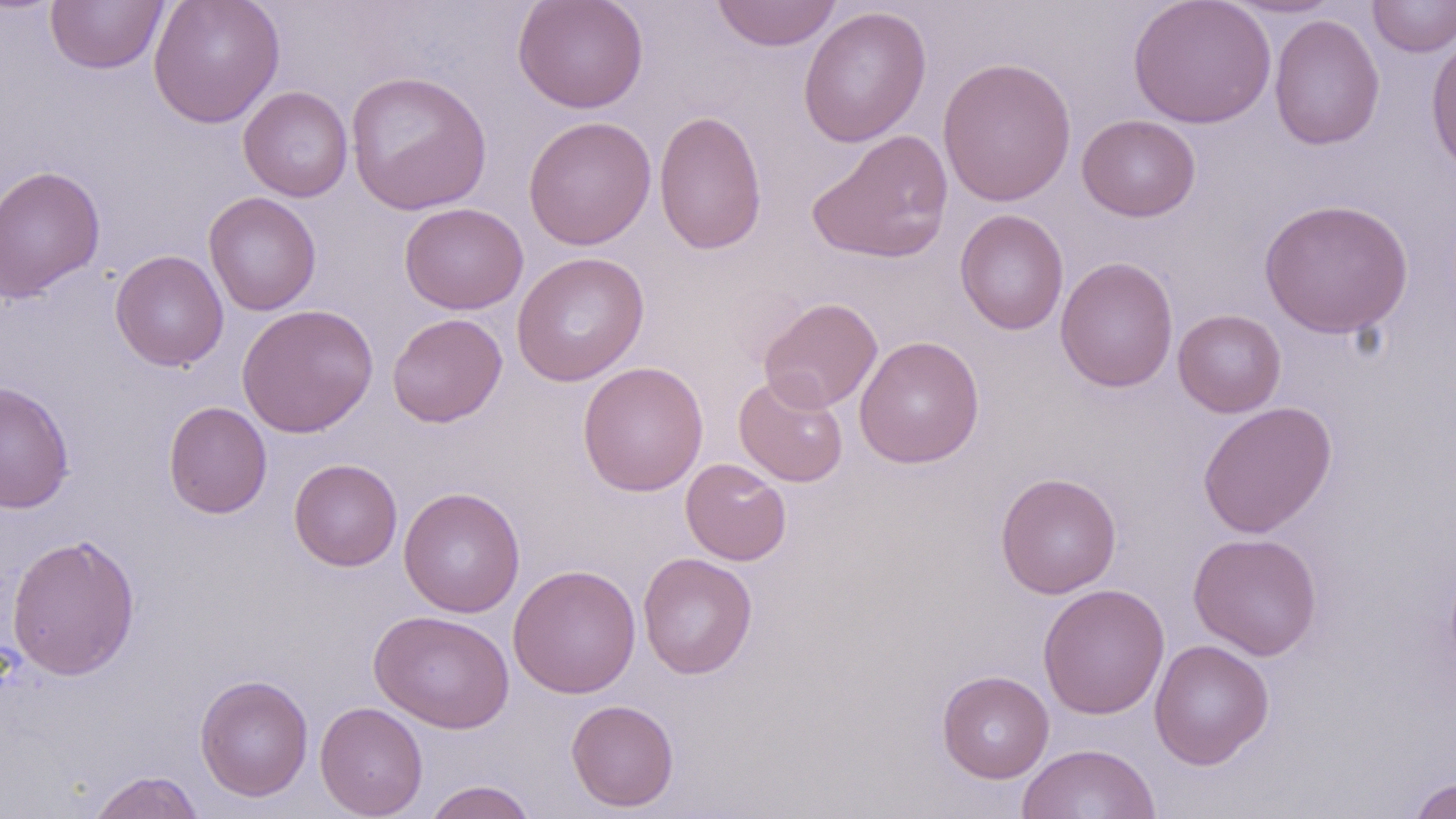 Approximate bounding boxes as [x1, y1, x2, y2] in pixels. Uninfected red blood cell locations: [148, 0, 285, 127], [513, 0, 649, 114], [710, 0, 843, 51], [1128, 0, 1276, 128], [1223, 0, 1343, 19], [1367, 0, 1456, 57], [46, 1, 168, 74], [797, 6, 932, 147], [1269, 14, 1385, 150], [1425, 34, 1456, 179], [937, 56, 1076, 207], [345, 70, 492, 215], [238, 85, 353, 202], [653, 109, 768, 256], [1077, 114, 1201, 222], [523, 115, 656, 251], [807, 129, 954, 265], [0, 164, 105, 303], [204, 192, 321, 316], [1259, 198, 1414, 338], [399, 202, 528, 315], [954, 209, 1069, 335], [110, 250, 229, 371], [511, 252, 650, 386], [1055, 256, 1179, 393], [758, 297, 883, 413], [237, 303, 378, 438], [1173, 309, 1286, 417], [387, 313, 507, 427], [854, 335, 984, 469], [577, 361, 709, 497], [734, 374, 848, 487], [0, 379, 75, 514], [164, 401, 272, 518], [1197, 401, 1337, 538], [289, 458, 402, 571], [680, 458, 792, 565], [995, 473, 1122, 599], [399, 486, 525, 617], [6, 532, 141, 681], [1187, 532, 1323, 660], [637, 552, 758, 679], [508, 564, 642, 699], [1038, 583, 1170, 719], [369, 610, 515, 734], [1149, 639, 1275, 769], [936, 670, 1054, 783], [194, 673, 313, 802], [566, 699, 679, 811], [315, 701, 428, 818], [1016, 742, 1160, 819], [87, 770, 206, 819], [1407, 776, 1456, 819], [423, 780, 538, 819]. Slide-level diagnosis: no evidence of blood parasites. Thin blood smear. Captured at 1000x magnification. Single field of view. Optical microscopy. Image is 1456×819 pixels. May-Grünwald-Giemsa-stained preparation.